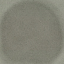

Result: no malaria parasites seen. Thin blood film. Acquired by smartphone through the microscope eyepiece. Giemsa stain. Cell patch, automatically extracted from a larger field of view and resized to 64 × 64 pixels.